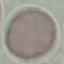
malaria_status: uninfected
stain: Giemsa
image_type: automatically extracted cell patch, resized to 64 × 64 pixels
capture: smartphone camera at the microscope eyepiece
preparation: thin blood smear